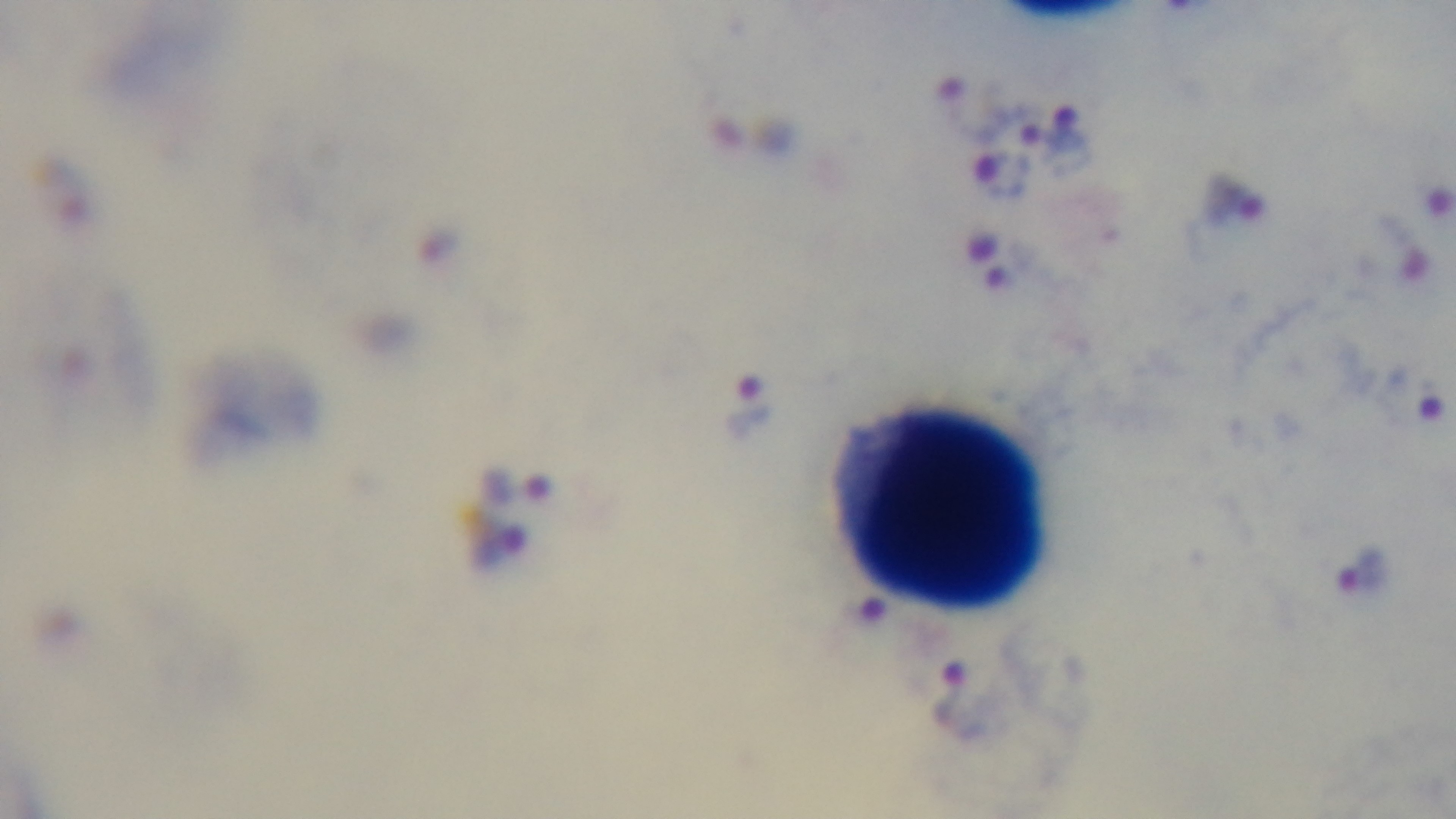
Summary:
  - Capture: mounted 4K digital camera
  - Objective: 100x oil immersion
  - Malaria status: positive
  - Preparation: thick
  - Stain: Giemsa
  - Field of view: single
  - Modality: light microscopy